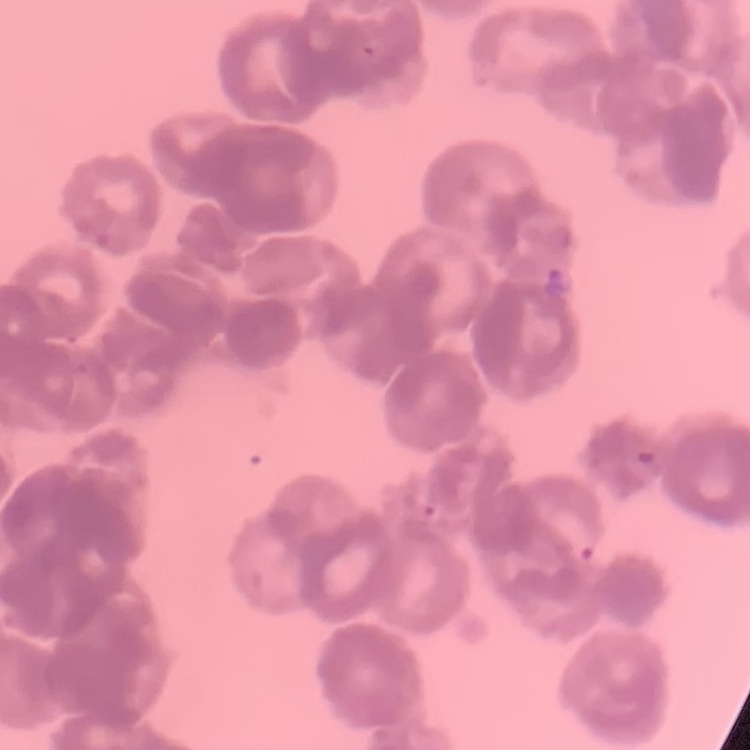
The red blood cells exhibit rouleaux formation. Thin blood smear. Field's or Giemsa stain. One tile cut from a larger photomicrograph.